Evaluate for Plasmodium parasites.
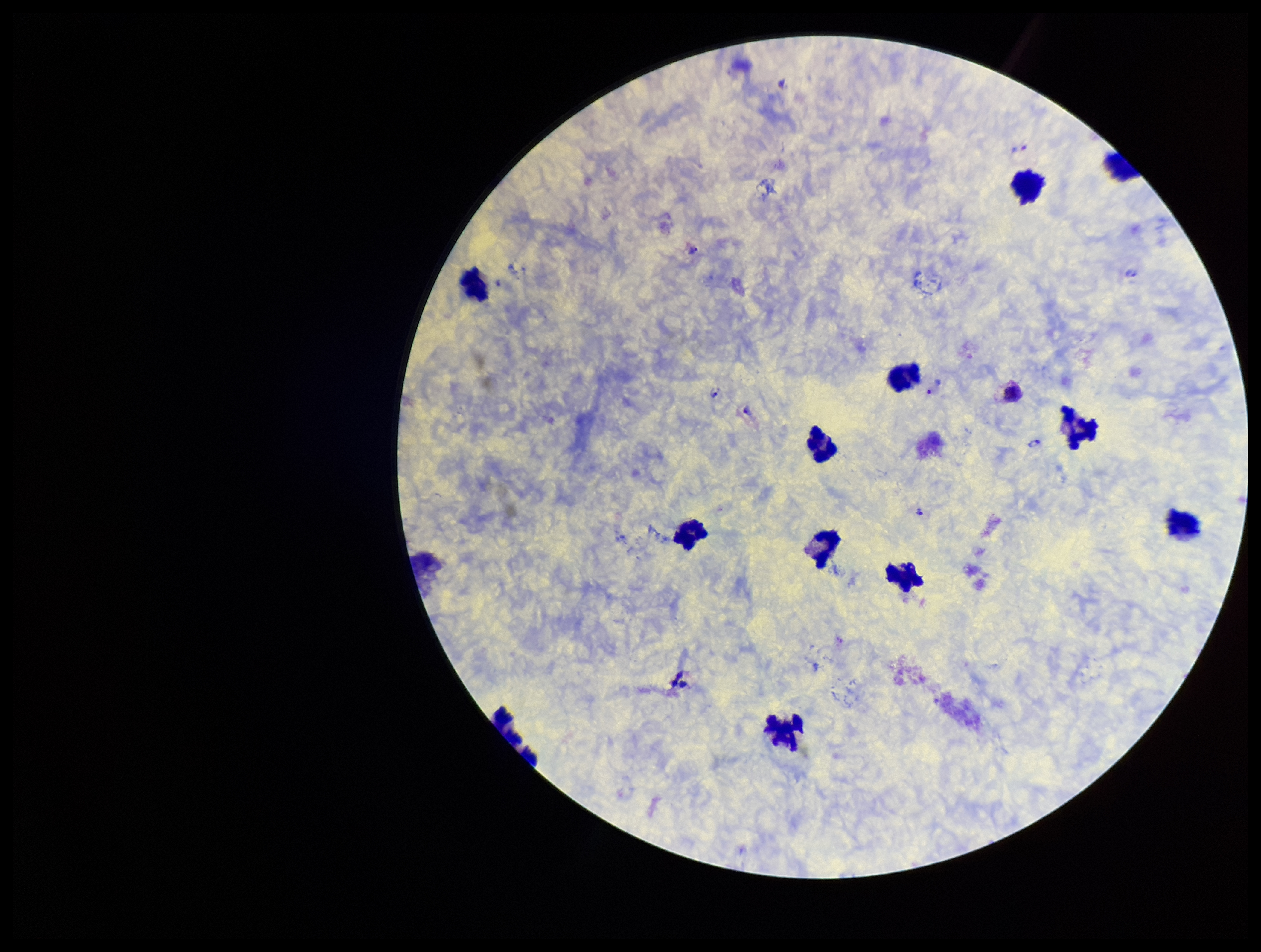

Detected.

Image is 1261×952 pixels. Stained with Giemsa. Preparation: thick blood smear. Single field of view. Leukocyte count: 13. Patient malaria status: positive. Photographed through the microscope eyepiece with a smartphone camera. Species reported for this patient: Plasmodium vivax. Parasite count: 9.